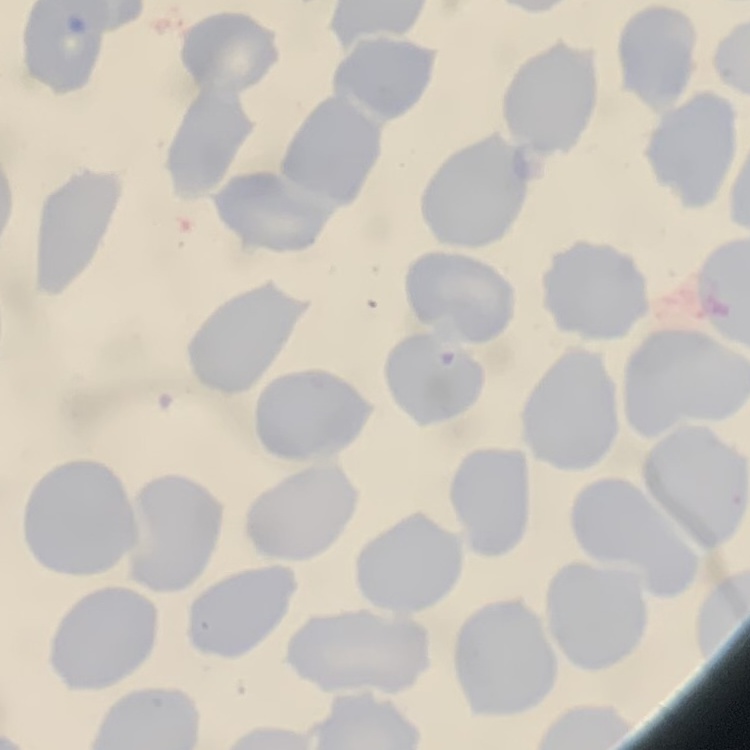 The red blood cells exhibit no rouleaux formation. One tile cut from a larger photomicrograph. Thin peripheral smear. Stained with either Field's or Giemsa.